Locate every Plasmodium ovale-infected red blood cell.
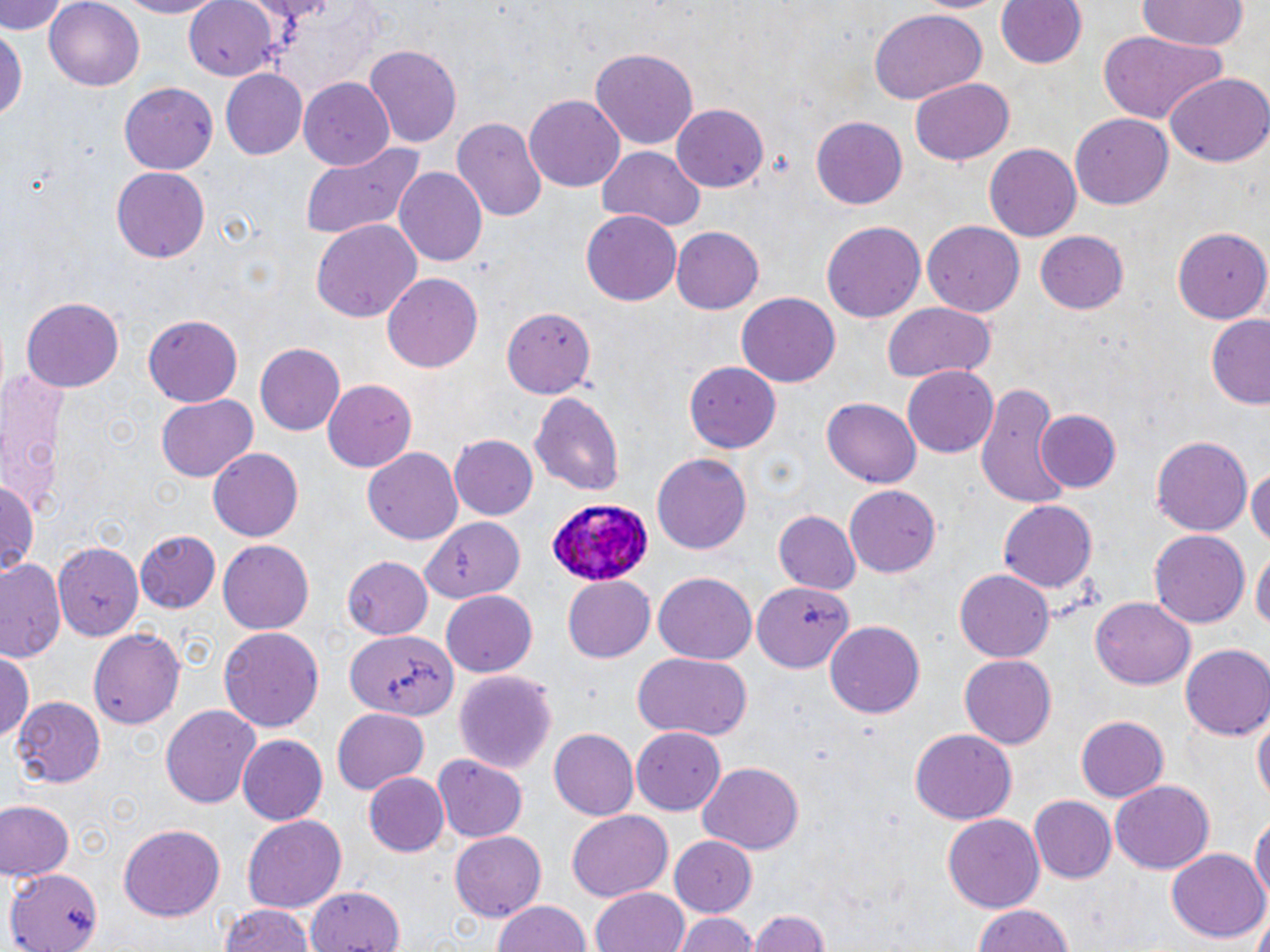
Approximate bounding boxes as [x1, y1, x2, y2] in pixels.
Plasmodium ovale-infected red blood cells: [543, 498, 653, 584].

Uninfected red blood cell locations: [1, 0, 69, 35], [107, 0, 227, 18], [184, 0, 277, 79], [994, 0, 1087, 72], [1133, 0, 1249, 52], [45, 1, 147, 89], [868, 9, 985, 105], [0, 24, 25, 128], [1098, 31, 1229, 126], [363, 43, 464, 150], [590, 45, 699, 150], [219, 70, 306, 159], [1165, 72, 1270, 168], [910, 77, 1014, 167], [298, 78, 395, 170], [120, 82, 217, 175], [524, 94, 624, 192], [672, 104, 769, 192], [1070, 114, 1172, 211], [809, 115, 909, 213], [453, 116, 547, 225], [297, 142, 425, 240], [985, 144, 1082, 241], [597, 146, 705, 231], [111, 166, 209, 263], [392, 168, 486, 268], [581, 209, 683, 306], [311, 219, 422, 323], [821, 220, 926, 323], [923, 222, 1025, 317], [1175, 224, 1270, 323], [672, 227, 764, 313], [1036, 231, 1129, 315], [382, 273, 483, 373], [736, 292, 839, 388], [21, 297, 122, 394], [882, 302, 998, 383], [504, 307, 595, 399], [143, 314, 244, 405], [1205, 314, 1270, 411], [253, 342, 345, 436], [685, 361, 785, 451], [0, 364, 75, 518], [900, 365, 999, 459], [323, 379, 418, 473], [976, 386, 1068, 507], [529, 389, 626, 494], [155, 392, 258, 483], [821, 397, 922, 490], [1035, 408, 1122, 493], [449, 435, 537, 519], [1151, 435, 1253, 538], [208, 447, 303, 541], [362, 447, 464, 545], [650, 452, 752, 556], [1248, 462, 1270, 555], [0, 476, 39, 576], [843, 484, 941, 578], [1000, 499, 1096, 595], [773, 510, 862, 597], [423, 515, 524, 603], [1150, 529, 1250, 626], [136, 530, 221, 612], [55, 541, 142, 639], [217, 541, 312, 634], [1252, 547, 1269, 637], [342, 556, 433, 640], [1, 558, 65, 663], [654, 569, 756, 662], [955, 570, 1053, 660], [563, 574, 656, 662], [754, 580, 852, 674], [440, 590, 538, 677], [1089, 597, 1195, 690], [825, 621, 925, 719], [218, 626, 324, 732], [89, 627, 184, 732], [347, 630, 457, 718], [1181, 642, 1270, 741], [2, 649, 36, 742], [630, 651, 752, 743], [960, 654, 1057, 749], [452, 669, 558, 776], [12, 697, 106, 787], [161, 704, 260, 807], [1253, 706, 1268, 813], [331, 708, 428, 793], [1076, 715, 1169, 800], [548, 728, 639, 822], [631, 728, 728, 813], [909, 729, 1015, 825], [237, 734, 327, 823], [432, 754, 530, 841], [697, 763, 804, 853], [364, 771, 450, 857], [1110, 781, 1214, 874], [1028, 794, 1115, 881], [1, 799, 74, 879], [567, 810, 675, 902], [943, 813, 1045, 913], [1251, 813, 1270, 913], [241, 816, 346, 914], [118, 825, 224, 919], [450, 831, 546, 920], [668, 836, 758, 917], [1167, 849, 1268, 943], [9, 865, 106, 952], [305, 884, 408, 952], [593, 889, 692, 952], [492, 899, 594, 952], [215, 903, 319, 952], [972, 903, 1076, 952], [749, 908, 828, 952], [672, 912, 756, 952]. Slide-level diagnosis: Plasmodium ovale. Single field of view. 1000x magnification. May-Grünwald-Giemsa-stained preparation. Light microscopy. Thin blood smear. Image is 1270×952 pixels.